Describe the morphology of the red blood cells.
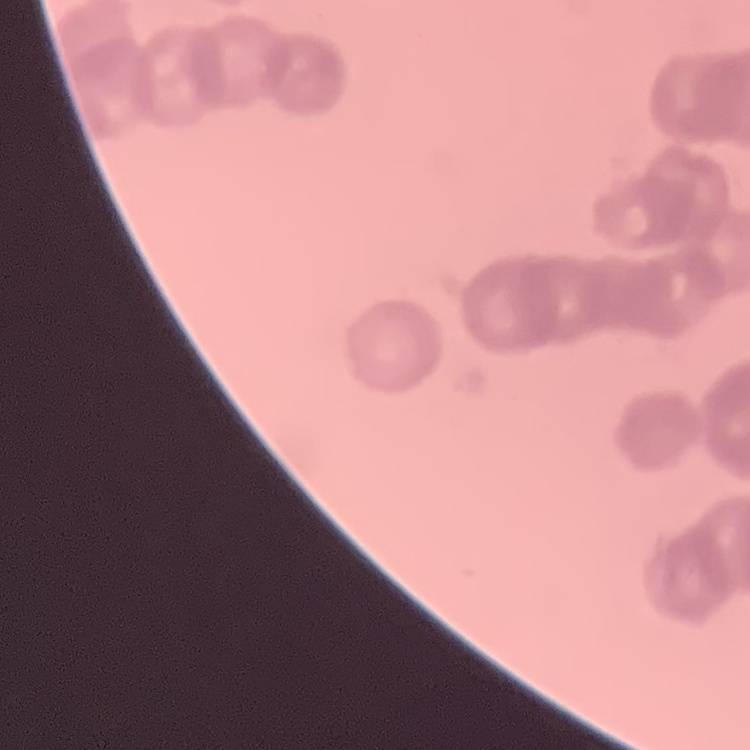
They show rouleaux formation.

Summary:
  - Stain: Field's or Giemsa
  - Image type: square crop of a larger photomicrograph
  - Preparation: thin peripheral smear